Identify the preparation type.
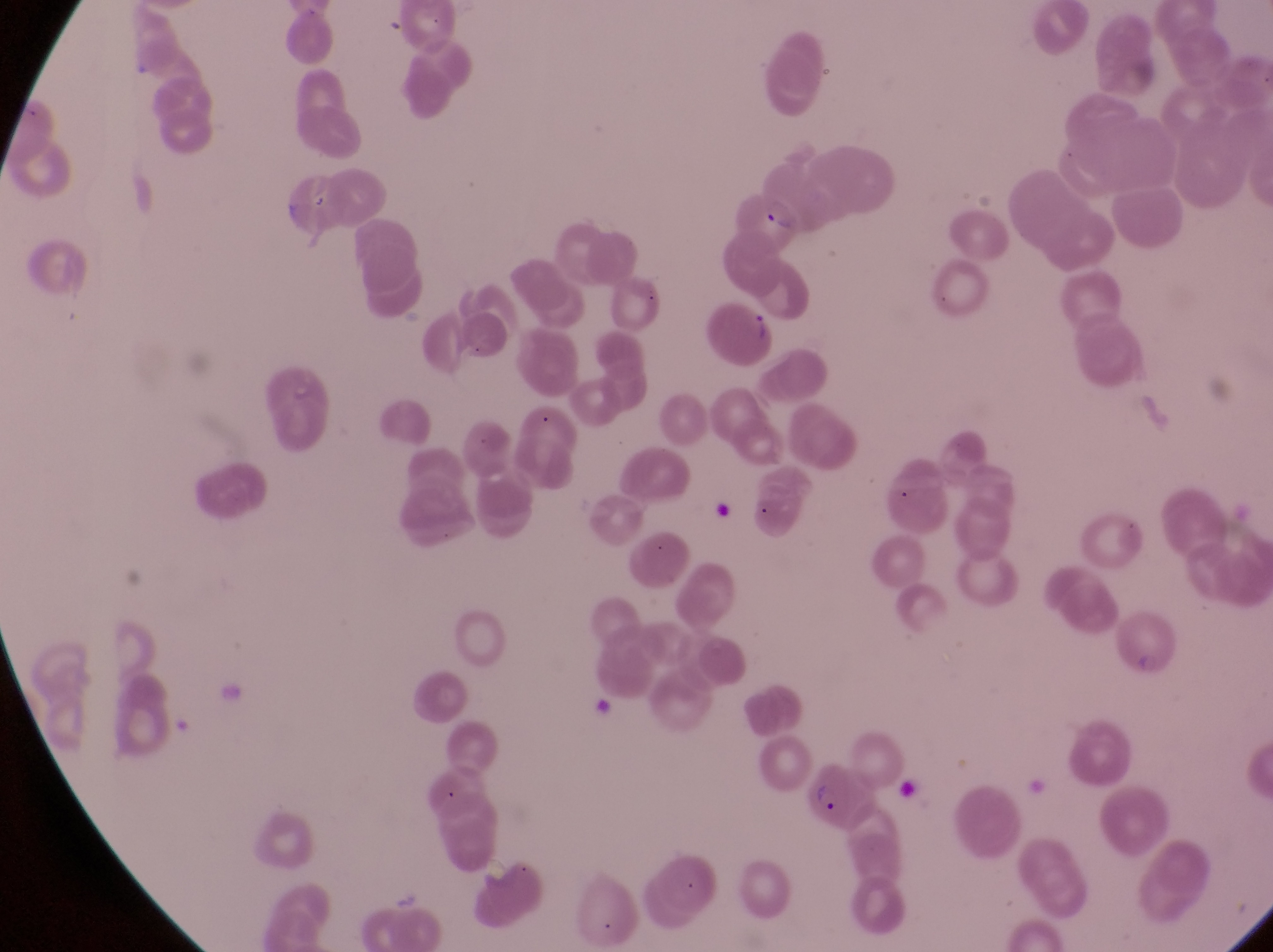

Thin blood smear.

Approximate bounding boxes as left top right bottom in pixels.
Summary:
  - Parasitised red blood cell locations: 708 294 783 369; 808 764 880 832
  - Capture: smartphone photograph through the eyepiece of an Olympus CX-23 microscope
  - Magnification: 1000x
  - Field of view: single
  - Country: Uganda
  - Image size: 1273×952 pixels